Give the position of every malaria parasite.
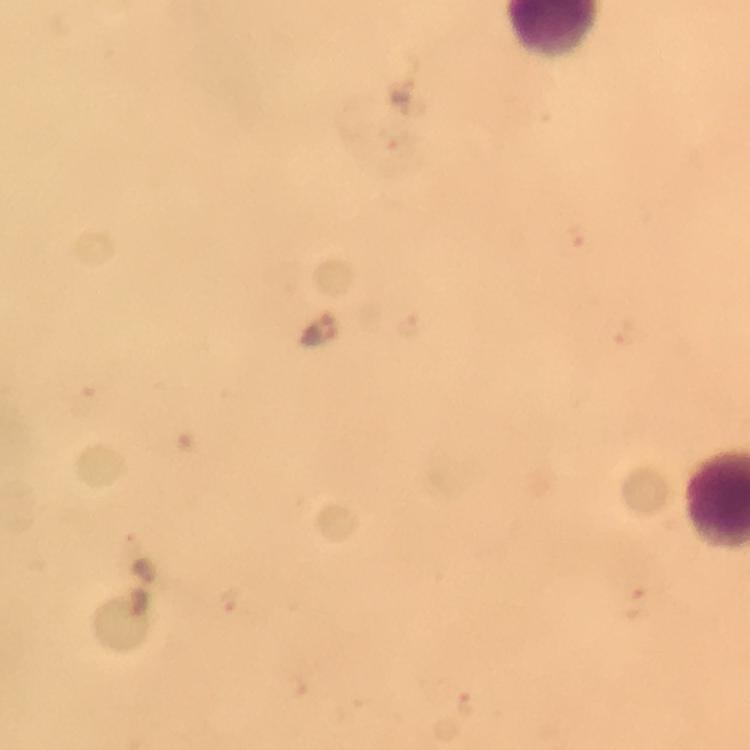

Approximate centers as {x, y} in pixels.
Malaria parasites: {320, 331}.

Summary:
  - Context: from a malaria diagnostic workup
  - Cropped from: a single field of view
  - Stain: Giemsa
  - Image size: 750×750 pixels
  - Magnification: 100x
  - Preparation: thick blood smear
  - Immersion oil: applied
  - Capture: smartphone mounted on the microscope